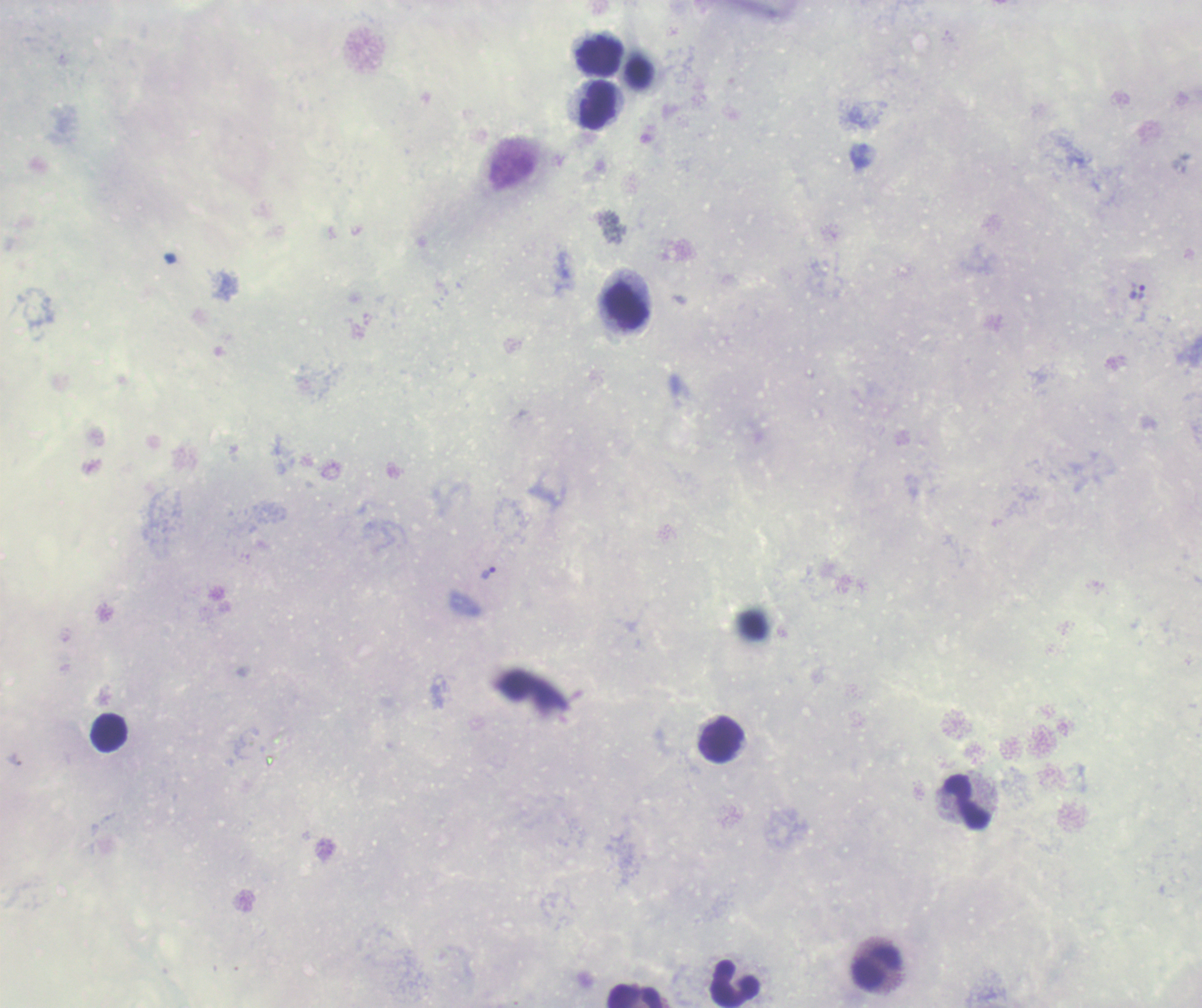
Approximate centers as [x, y] in pixels.
Summary:
  - Trophozoite locations: [1136, 290], [489, 573]
  - Leukocyte locations: [599, 56], [598, 105], [626, 306], [109, 732], [722, 739], [968, 802], [876, 968], [734, 983], [635, 996]
  - Coloration quality: bad
  - Image size: 1202×1008 pixels
  - Result: positive for malaria parasites
  - Preparation: thick blood smear
  - Background quality: poor
  - Stain: Romanowsky
  - Field of view: one from this slide
  - Magnification: 100x
  - Context: previously used in a real diagnosis